Identify the parasite.
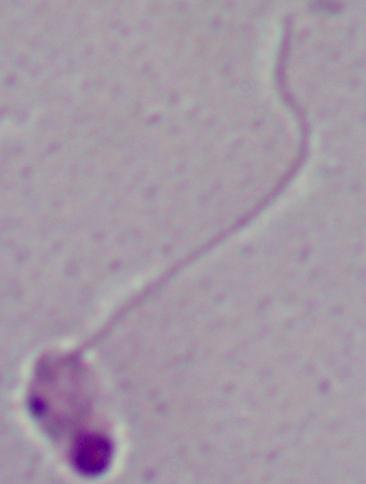

This is Leishmania.

{
  "modality": "photomicrograph",
  "magnification": "1000x"
}